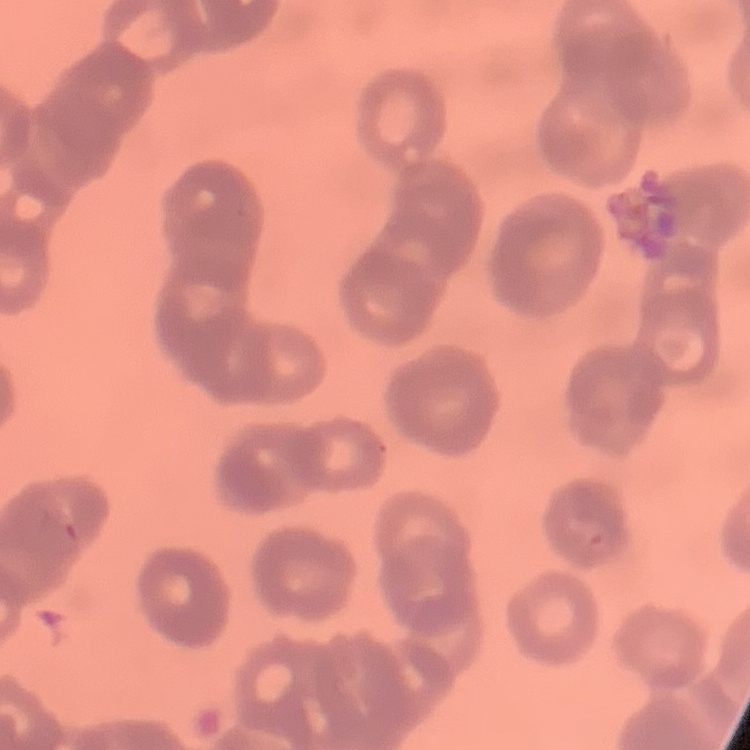 The erythrocytes show rouleaux formation. Field's or Giemsa stain. One tile cut from a larger photomicrograph. Thin blood film.